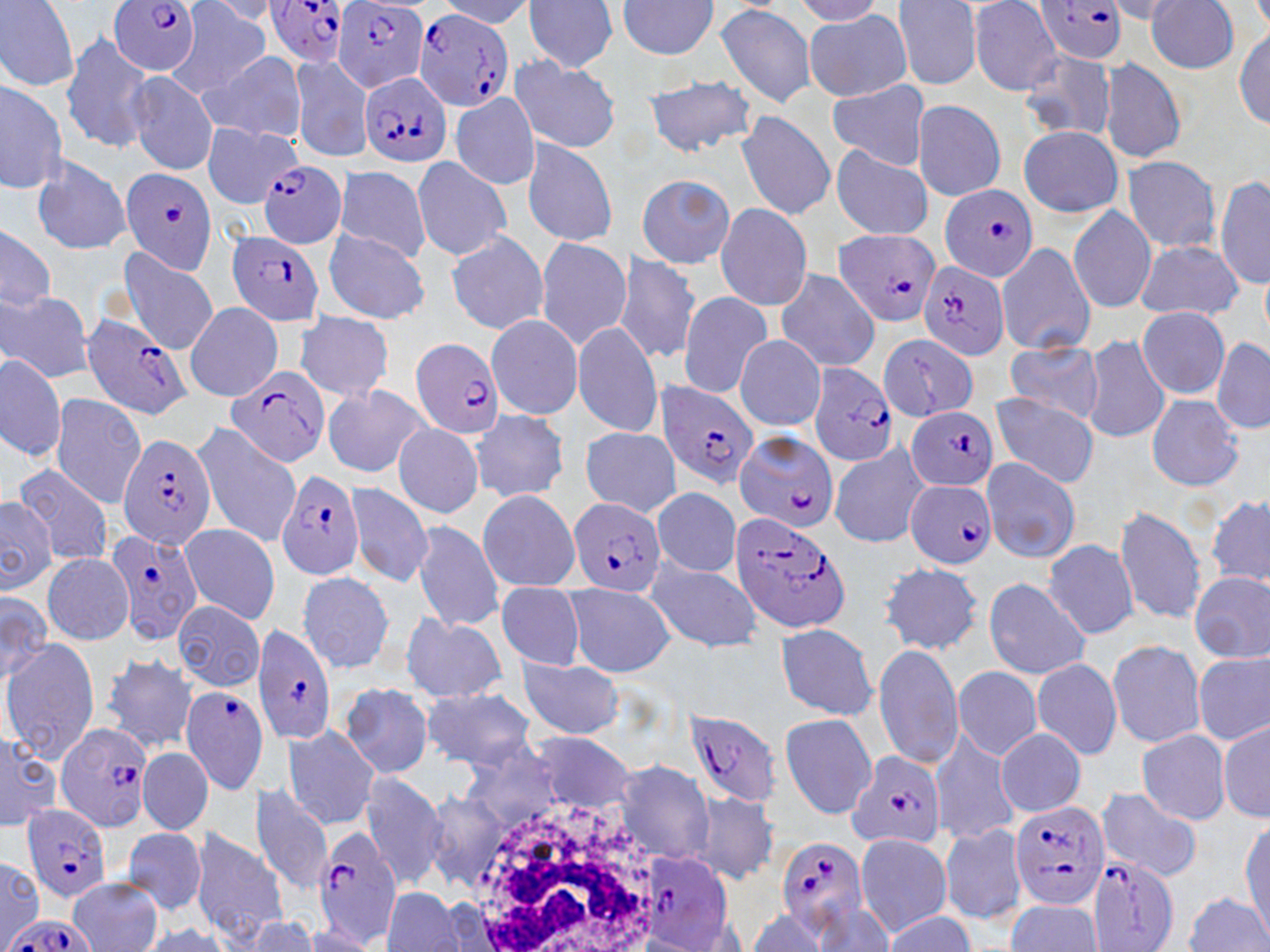
Approximate bounding boxes as [x1, y1, x2, y2] in pixels. White blood cell locations: [462, 795, 670, 952]. Uninfected red blood cell locations: [436, 0, 537, 29], [523, 0, 619, 74], [789, 0, 887, 25], [0, 1, 79, 90], [197, 1, 285, 24], [616, 1, 722, 60], [893, 1, 982, 90], [967, 1, 1063, 95], [1146, 1, 1244, 73], [1103, 2, 1191, 25], [715, 3, 819, 110], [167, 4, 271, 99], [804, 8, 913, 102], [1234, 24, 1269, 129], [61, 32, 155, 152], [1017, 50, 1117, 143], [199, 52, 308, 145], [289, 54, 376, 162], [509, 54, 622, 154], [1098, 56, 1187, 165], [125, 71, 219, 175], [645, 74, 755, 156], [0, 77, 67, 195], [828, 82, 930, 169], [450, 91, 539, 190], [911, 99, 1007, 202], [737, 112, 835, 221], [201, 122, 302, 208], [1018, 125, 1123, 217], [520, 137, 619, 248], [831, 145, 933, 240], [30, 154, 132, 256], [1121, 155, 1221, 252], [411, 157, 513, 263], [333, 164, 431, 264], [1216, 174, 1269, 290], [636, 176, 735, 268], [713, 203, 814, 311], [1068, 205, 1157, 314], [0, 223, 55, 318], [323, 230, 430, 324], [446, 230, 549, 334], [534, 237, 633, 351], [995, 240, 1096, 356], [1135, 240, 1244, 319], [118, 246, 220, 355], [614, 253, 702, 366], [773, 267, 882, 372], [1, 291, 93, 381], [677, 291, 771, 397], [184, 302, 284, 401], [1138, 306, 1230, 399], [293, 312, 395, 402], [485, 313, 582, 421], [572, 322, 664, 437], [735, 336, 825, 430], [1083, 336, 1169, 446], [1211, 339, 1270, 435], [1001, 342, 1106, 423], [0, 353, 65, 461], [321, 383, 432, 479], [988, 393, 1100, 488], [47, 394, 149, 508], [1146, 395, 1244, 491], [470, 409, 571, 504], [392, 421, 484, 518], [191, 424, 301, 547], [579, 426, 681, 515], [829, 442, 930, 548], [980, 457, 1082, 564], [12, 462, 117, 567], [344, 483, 435, 587], [651, 486, 741, 578], [477, 489, 580, 590], [2, 493, 58, 595], [1206, 496, 1270, 592], [1114, 505, 1207, 626], [412, 519, 504, 631], [177, 522, 281, 624], [1043, 539, 1140, 639], [41, 553, 132, 645], [641, 556, 764, 654], [876, 561, 985, 656], [295, 570, 395, 675], [1189, 570, 1270, 662], [983, 577, 1090, 679], [497, 582, 584, 671], [563, 584, 674, 676], [0, 589, 50, 689], [172, 600, 265, 691], [401, 612, 506, 705], [772, 624, 880, 722], [1106, 639, 1206, 747], [1, 641, 101, 767], [872, 641, 962, 769], [1192, 650, 1269, 745], [99, 652, 198, 751], [515, 656, 625, 738], [1030, 658, 1122, 759], [953, 666, 1043, 760], [339, 681, 434, 779], [419, 686, 537, 769], [779, 712, 878, 817], [1219, 720, 1269, 822], [281, 726, 381, 829], [0, 728, 61, 834], [929, 728, 1020, 845], [996, 728, 1086, 816], [1135, 729, 1232, 824], [527, 733, 637, 812], [462, 741, 565, 831], [137, 746, 213, 835], [613, 761, 715, 867], [359, 774, 447, 890], [249, 784, 334, 894], [1093, 788, 1202, 882], [689, 790, 781, 884], [421, 791, 509, 891], [203, 803, 335, 929], [1240, 819, 1269, 934], [941, 824, 1028, 925], [123, 827, 207, 916], [188, 829, 290, 944], [854, 833, 952, 935], [0, 856, 42, 946], [65, 876, 163, 952], [381, 887, 466, 952], [1184, 892, 1270, 951], [801, 898, 895, 952], [1005, 900, 1105, 951], [744, 910, 834, 952], [882, 912, 978, 950], [235, 913, 321, 951], [128, 921, 235, 952], [297, 926, 383, 951]. Plasmodium falciparum-infected red blood cell locations: [110, 0, 202, 76], [262, 0, 354, 68], [1031, 0, 1129, 64], [333, 2, 429, 95], [413, 8, 516, 108], [360, 72, 452, 169], [254, 159, 347, 248], [120, 167, 219, 274], [940, 184, 1040, 281], [834, 227, 939, 329], [225, 230, 325, 327], [916, 259, 1010, 361], [76, 309, 192, 421], [878, 335, 978, 420], [411, 336, 507, 439], [807, 362, 897, 467], [225, 369, 331, 468], [658, 379, 758, 489], [906, 405, 999, 490], [735, 430, 838, 534], [118, 434, 216, 548], [276, 469, 367, 583], [905, 481, 996, 568], [567, 495, 668, 598], [727, 509, 854, 635], [105, 527, 205, 646], [252, 624, 337, 748], [180, 684, 271, 795], [684, 710, 781, 807], [53, 721, 156, 834], [846, 751, 947, 850], [1010, 799, 1109, 910], [22, 803, 115, 903], [313, 827, 405, 948], [776, 837, 866, 932], [636, 851, 737, 948], [1088, 853, 1181, 951], [1, 915, 101, 952]. Slide-level diagnosis: Plasmodium falciparum. Light microscopy. Image is 1270×952 pixels. May-Grünwald-Giemsa-stained preparation. Thin blood smear. Captured at 1000x magnification. One field of a larger specimen.